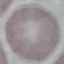

malaria_status: uninfected
preparation: thin blood film
capture: smartphone camera at the microscope eyepiece
image_type: automatically extracted cell patch, resized to 64 × 64 pixels
stain: Giemsa